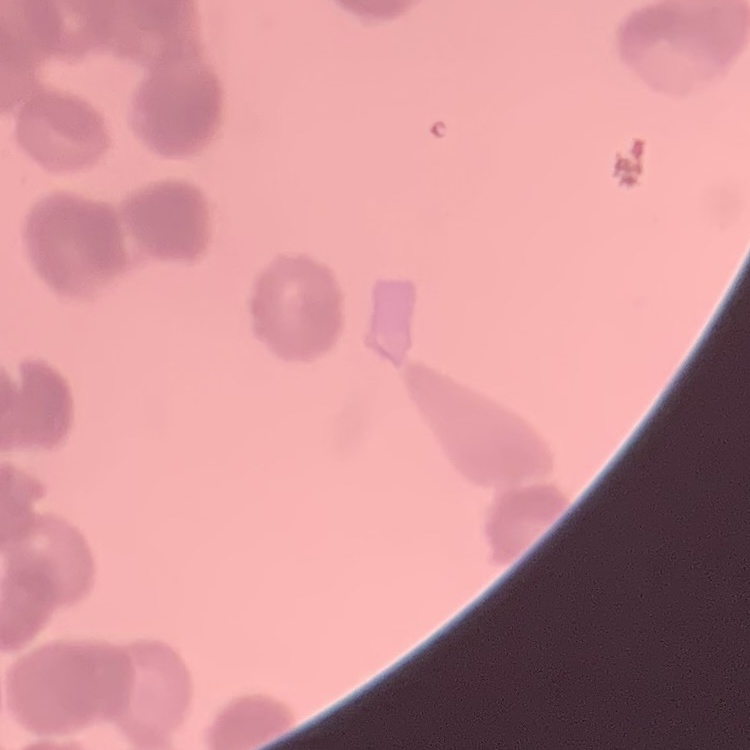
{
  "red_blood_cell_morphology": "rouleaux formation",
  "image_type": "one tile cut from a larger photomicrograph",
  "preparation": "thin blood film",
  "stain": "Field's or Giemsa"
}